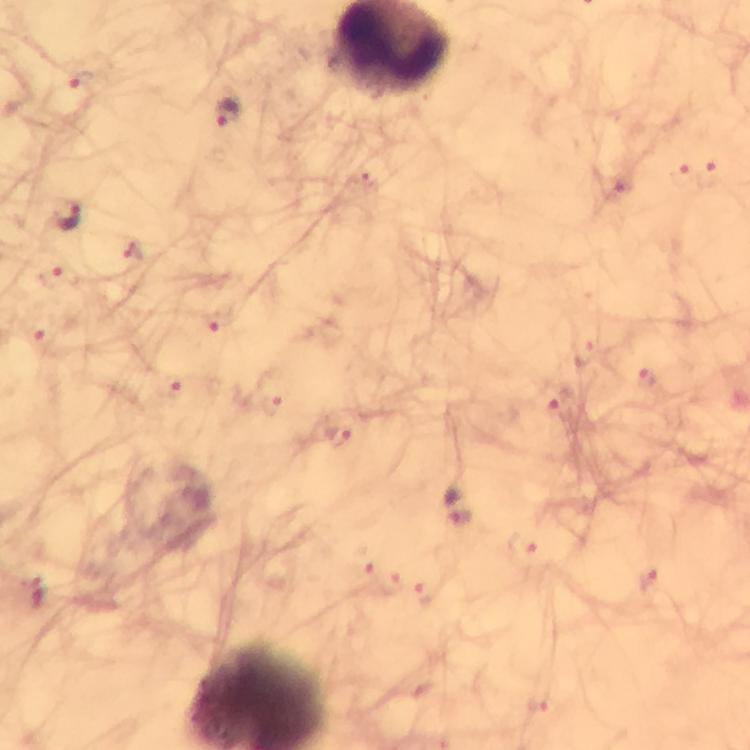
immersion oil = applied
stain = Giemsa
capture = smartphone camera through the microscope
image size = 750×750 pixels
magnification = 100x
cropped from = one field of view
context = from a malaria diagnostic workup
preparation = thick blood film
malaria parasite locations = approximate object centers, in pixels from the top-left corner: (x=229, y=115), (x=69, y=217), (x=459, y=504)